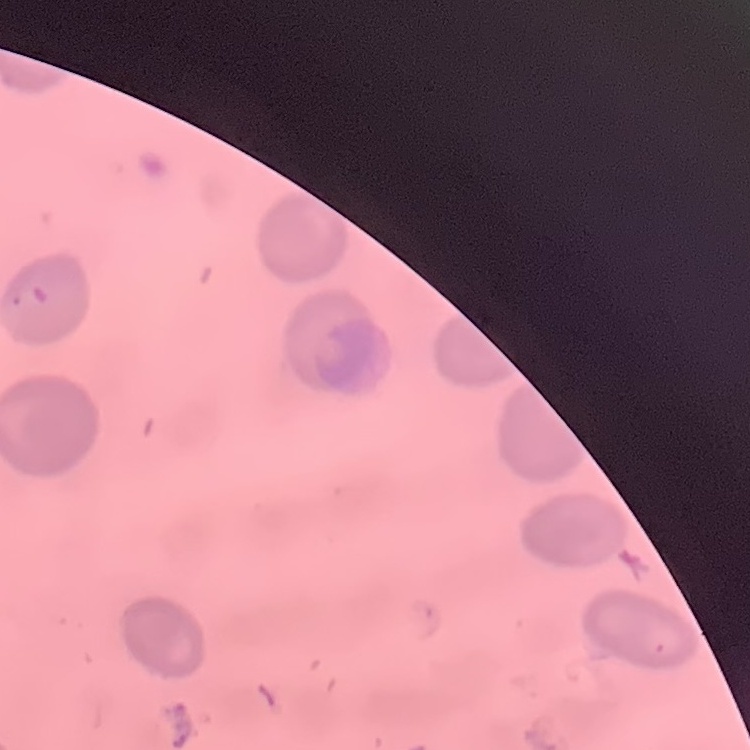
Summary:
  - Red blood cell morphology: no rouleaux formation
  - Preparation: thin blood film
  - Stain: Field's or Giemsa
  - Image type: one tile cut from a larger photomicrograph